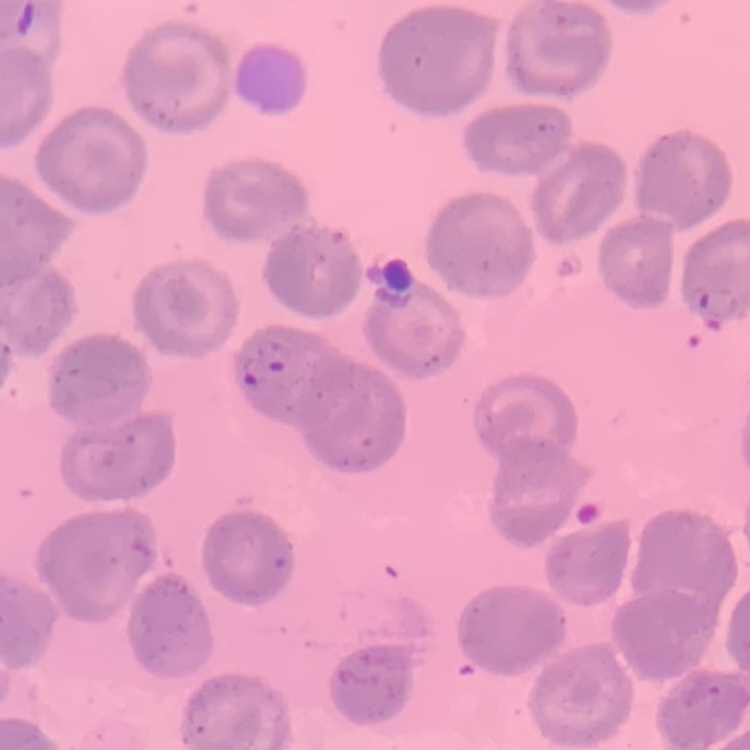
The erythrocytes exhibit no rouleaux formation. Thin peripheral smear. Square crop of a larger photomicrograph. Field's or Giemsa stain.